Locate and identify every blood parasite.
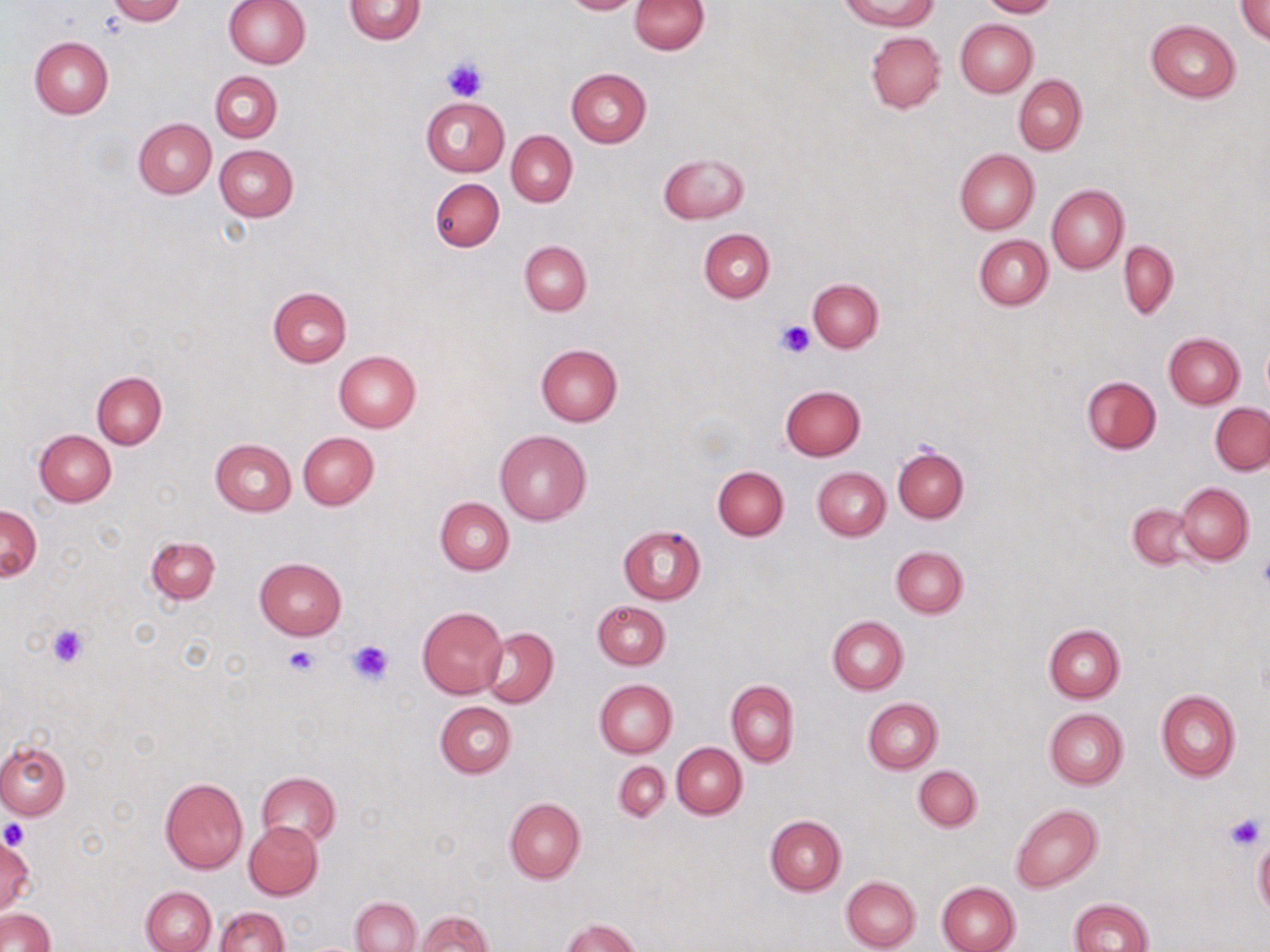
No blood parasites seen.

slide_level_diagnosis: negative for blood parasites
uninfected_red_blood_cell_locations: 'approximate bounding boxes as [x1, y1, x2, y2] in pixels: [108, 0, 186, 24], [222, 0, 310, 69], [344, 0, 426, 44], [560, 0, 642, 15], [629, 0, 709, 54], [840, 0, 940, 30], [980, 0, 1058, 18], [1235, 1, 1270, 43], [955, 19, 1037, 97], [1146, 19, 1241, 102], [865, 31, 946, 114], [29, 36, 113, 118], [565, 67, 651, 147], [210, 72, 281, 142], [1013, 75, 1087, 155], [421, 96, 509, 177], [133, 118, 217, 198], [506, 131, 578, 207], [215, 145, 298, 221], [955, 148, 1039, 234], [658, 152, 749, 223], [429, 178, 504, 252], [1045, 184, 1128, 272], [699, 228, 774, 303], [973, 236, 1052, 310], [520, 241, 591, 315], [1118, 241, 1178, 318], [808, 278, 883, 351], [267, 286, 352, 367], [1165, 333, 1244, 408], [1262, 334, 1270, 402], [535, 343, 623, 427], [333, 351, 421, 433], [91, 371, 167, 448], [1081, 376, 1161, 453], [779, 386, 865, 461], [1210, 403, 1270, 475], [34, 430, 116, 506], [495, 430, 591, 526], [297, 431, 379, 510], [209, 438, 297, 515], [893, 446, 968, 523], [712, 466, 789, 540], [813, 467, 890, 539], [1175, 482, 1254, 566], [434, 497, 513, 574], [1126, 505, 1198, 571], [1, 506, 42, 581], [618, 525, 705, 604], [146, 535, 220, 603], [891, 546, 968, 618], [254, 557, 347, 640], [592, 600, 670, 669], [417, 606, 507, 698], [827, 616, 908, 694], [1043, 623, 1125, 701], [479, 627, 558, 708], [594, 680, 677, 758], [726, 681, 799, 767], [1156, 689, 1241, 782], [863, 698, 942, 773], [434, 701, 517, 779], [1044, 709, 1127, 789], [0, 740, 70, 819], [672, 743, 747, 819], [613, 761, 670, 822], [913, 764, 982, 830], [256, 771, 340, 845], [160, 777, 247, 873], [504, 798, 585, 884], [1011, 804, 1103, 892], [765, 814, 846, 895], [243, 821, 323, 900], [0, 835, 33, 916], [1253, 836, 1270, 917], [840, 875, 922, 951], [937, 880, 1020, 952], [142, 886, 216, 952], [350, 897, 421, 951], [1069, 898, 1155, 952], [214, 905, 288, 952], [1, 909, 55, 951], [413, 911, 493, 951], [562, 919, 642, 952]'
field_of_view: one of a larger specimen
image_size: 1270×952 pixels
stain: May-Grünwald-Giemsa
magnification: 1000x
modality: light microscopy
preparation: thin blood smear
platelet_locations: 'approximate bounding boxes as [x1, y1, x2, y2] in pixels: [442, 58, 487, 102], [776, 319, 815, 360], [1257, 552, 1270, 591], [45, 621, 93, 668], [347, 638, 394, 684], [283, 645, 320, 678], [1225, 812, 1266, 852], [1, 821, 30, 849]'